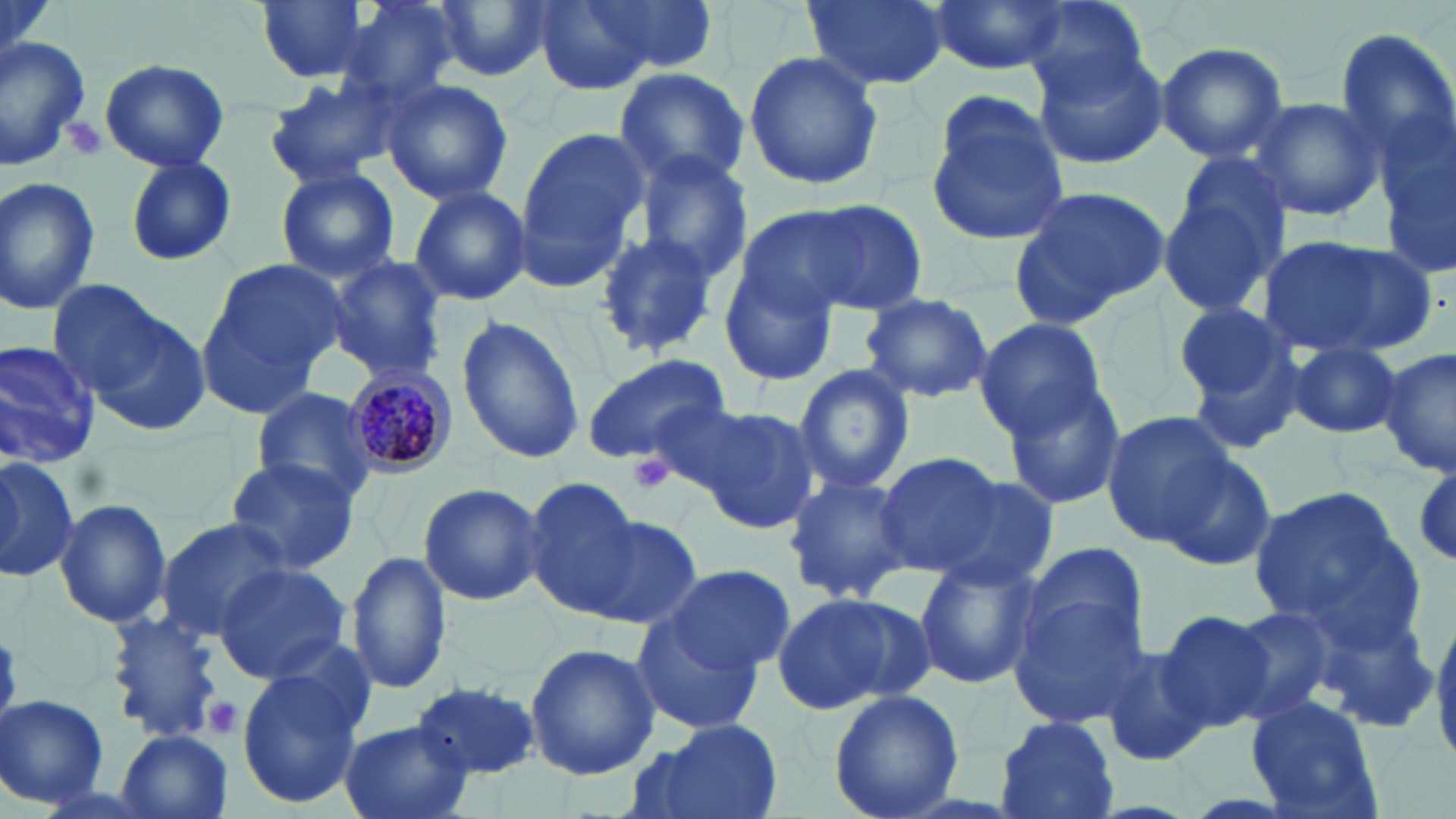
Approximate bounding boxes as (x1, y1, x2, y2) in pixels. Plasmodium malariae-infected red blood cell locations: (342, 366, 456, 475). Uninfected red blood cell locations: (256, 0, 376, 83), (433, 0, 551, 83), (584, 0, 723, 76), (801, 0, 954, 93), (928, 0, 1064, 77), (331, 1, 462, 104), (530, 1, 658, 94), (1017, 2, 1154, 102), (1334, 27, 1456, 167), (0, 32, 97, 171), (1155, 40, 1290, 164), (1030, 44, 1171, 169), (741, 50, 884, 192), (99, 60, 230, 172), (614, 66, 752, 191), (262, 72, 406, 188), (380, 79, 513, 206), (924, 95, 1069, 247), (1246, 95, 1387, 222), (1375, 104, 1456, 267), (513, 126, 648, 283), (631, 150, 754, 284), (125, 157, 236, 267), (1157, 164, 1293, 319), (274, 167, 400, 282), (0, 176, 101, 314), (407, 184, 531, 307), (1012, 184, 1171, 320), (800, 200, 928, 315), (738, 207, 876, 313), (589, 230, 727, 361), (1259, 235, 1437, 357), (720, 254, 840, 386), (324, 255, 448, 383), (194, 259, 344, 419), (67, 290, 213, 435), (860, 293, 993, 403), (1167, 301, 1308, 442), (456, 314, 586, 465), (973, 320, 1107, 439), (1285, 340, 1405, 439), (0, 341, 101, 465), (1380, 350, 1456, 477), (581, 352, 732, 466), (793, 364, 915, 495), (1000, 380, 1128, 511), (251, 390, 378, 502), (690, 405, 822, 534), (1101, 409, 1238, 546), (0, 452, 78, 578), (873, 452, 1003, 576), (1158, 452, 1276, 570), (224, 458, 363, 576), (929, 472, 1058, 590), (780, 473, 917, 606), (520, 476, 643, 617), (417, 482, 546, 607), (1246, 487, 1411, 636), (54, 496, 172, 628), (575, 511, 703, 633), (154, 518, 293, 644), (1019, 541, 1152, 670), (346, 549, 453, 696), (912, 553, 1040, 688), (212, 562, 353, 685), (660, 562, 795, 673), (1010, 589, 1154, 727), (772, 592, 925, 714), (1222, 604, 1342, 725), (1153, 608, 1279, 733), (632, 612, 767, 733), (102, 615, 223, 742), (1432, 616, 1456, 770), (525, 642, 661, 780), (1096, 643, 1214, 769), (234, 663, 368, 810), (410, 681, 541, 779), (828, 688, 965, 819), (1244, 694, 1383, 819), (0, 695, 110, 810), (993, 716, 1118, 819), (632, 719, 784, 819), (338, 720, 474, 819), (115, 728, 234, 819). Platelet locations: (61, 117, 107, 160), (628, 452, 673, 494), (201, 695, 244, 738). Slide-level diagnosis: Plasmodium malariae. Single field of view. May-Grünwald-Giemsa-stained preparation. Image is 1456×819 pixels. Thin blood smear. Captured at 1000x magnification. Light microscopy.